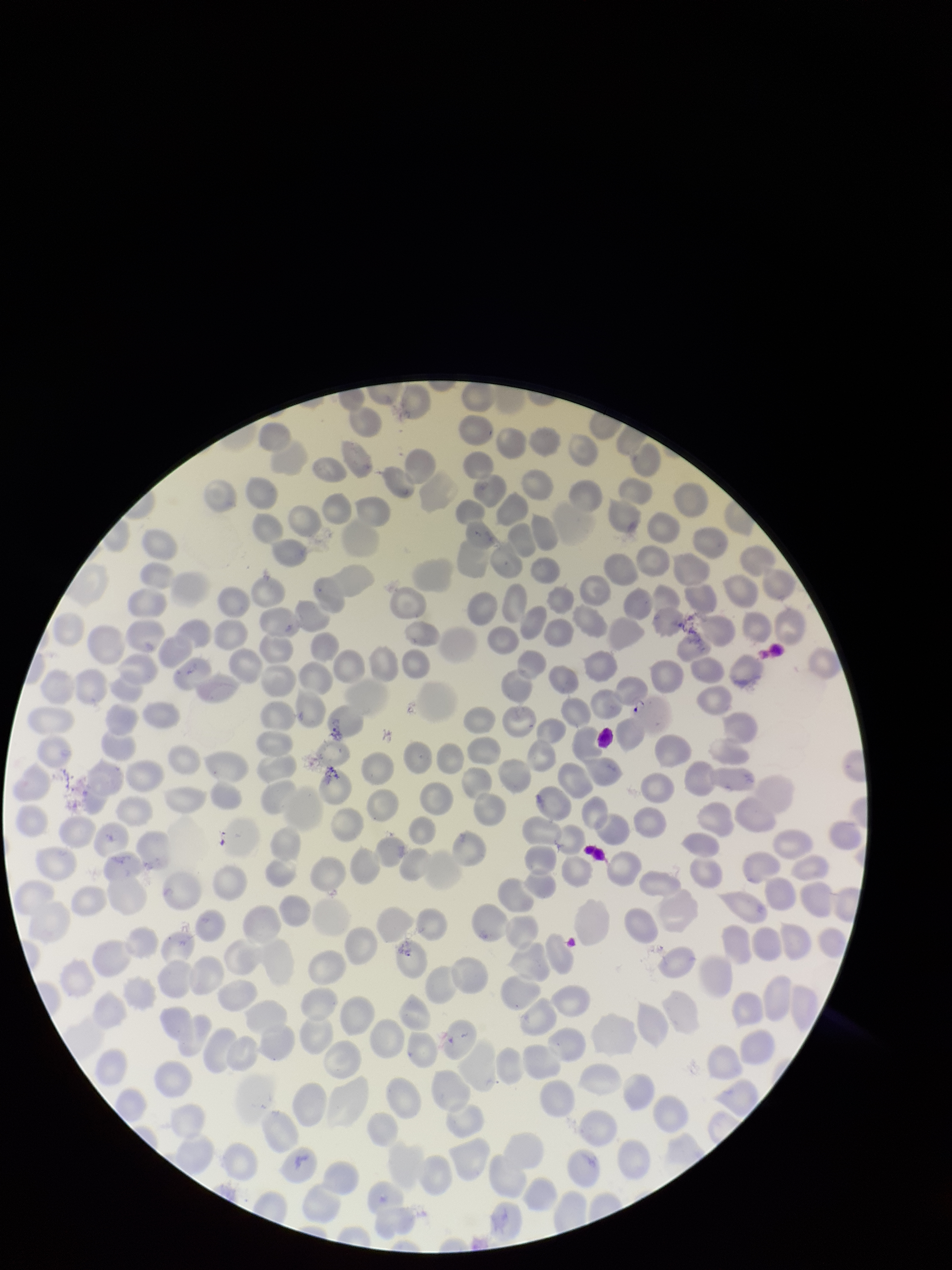
Preparation: thin. Photographed through the microscope eyepiece with a smartphone camera. Red blood cell count: 226. Parasitized red blood cells: none detected. Giemsa stain. Single field of view. Species reported for this patient: Plasmodium falciparum. Parasitized red blood cell count: 0. Image is 952×1270 pixels. Patient malaria status: infected.